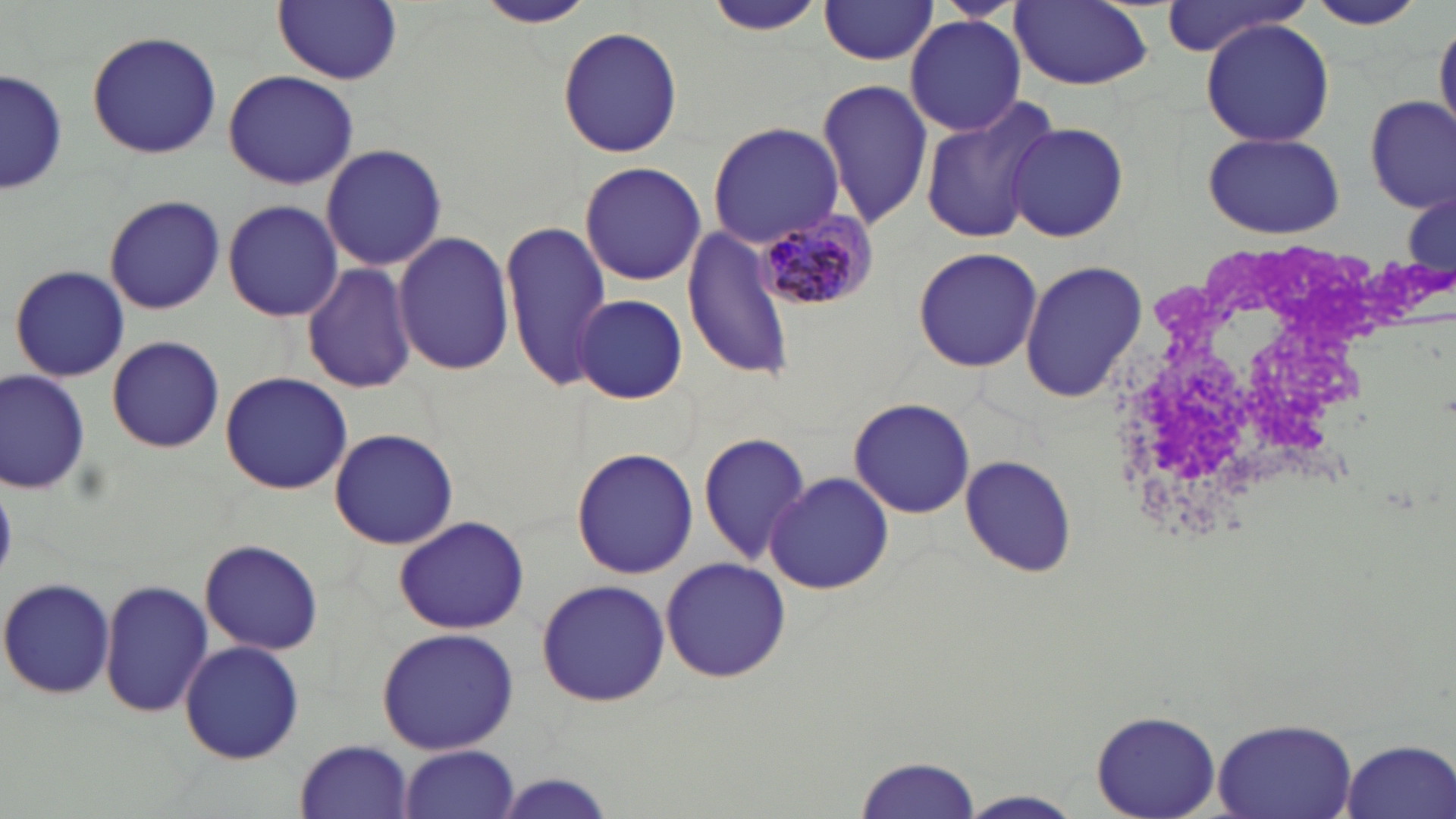 Approximate bounding boxes as named x1/y1/x2/y2 corners in pixels. Uninfected red blood cell locations: (x1=273, y1=0, x2=401, y2=86), (x1=1008, y1=0, x2=1155, y2=90), (x1=1301, y1=0, x2=1434, y2=32), (x1=478, y1=2, x2=596, y2=28), (x1=697, y1=2, x2=832, y2=36), (x1=817, y1=2, x2=939, y2=66), (x1=1158, y1=2, x2=1313, y2=61), (x1=904, y1=13, x2=1026, y2=136), (x1=1434, y1=15, x2=1456, y2=141), (x1=1201, y1=18, x2=1335, y2=148), (x1=557, y1=25, x2=683, y2=158), (x1=86, y1=29, x2=222, y2=159), (x1=2, y1=66, x2=65, y2=198), (x1=223, y1=69, x2=360, y2=191), (x1=815, y1=78, x2=936, y2=230), (x1=916, y1=96, x2=1061, y2=247), (x1=1364, y1=96, x2=1455, y2=214), (x1=706, y1=122, x2=845, y2=245), (x1=1006, y1=122, x2=1129, y2=243), (x1=1202, y1=130, x2=1347, y2=239), (x1=321, y1=142, x2=446, y2=273), (x1=578, y1=161, x2=707, y2=286), (x1=1402, y1=192, x2=1454, y2=276), (x1=103, y1=193, x2=225, y2=315), (x1=221, y1=199, x2=343, y2=321), (x1=499, y1=217, x2=612, y2=387), (x1=683, y1=229, x2=797, y2=383), (x1=392, y1=231, x2=515, y2=377), (x1=913, y1=245, x2=1042, y2=373), (x1=300, y1=261, x2=417, y2=394), (x1=1019, y1=261, x2=1148, y2=404), (x1=10, y1=265, x2=129, y2=383), (x1=575, y1=295, x2=686, y2=403), (x1=107, y1=335, x2=224, y2=453), (x1=0, y1=369, x2=89, y2=496), (x1=219, y1=371, x2=353, y2=496), (x1=848, y1=396, x2=977, y2=520), (x1=328, y1=426, x2=460, y2=548), (x1=697, y1=431, x2=810, y2=567), (x1=570, y1=446, x2=699, y2=579), (x1=959, y1=453, x2=1076, y2=578), (x1=763, y1=471, x2=892, y2=595), (x1=393, y1=515, x2=529, y2=635), (x1=198, y1=538, x2=326, y2=656), (x1=659, y1=557, x2=792, y2=684), (x1=0, y1=577, x2=118, y2=698), (x1=536, y1=577, x2=670, y2=708), (x1=99, y1=578, x2=214, y2=720), (x1=376, y1=628, x2=519, y2=754), (x1=180, y1=640, x2=304, y2=764), (x1=1092, y1=709, x2=1220, y2=818), (x1=1210, y1=715, x2=1360, y2=819), (x1=1337, y1=738, x2=1455, y2=818), (x1=296, y1=739, x2=415, y2=818), (x1=397, y1=745, x2=521, y2=819), (x1=854, y1=753, x2=983, y2=819), (x1=494, y1=773, x2=619, y2=819), (x1=957, y1=790, x2=1087, y2=818). Plasmodium malariae-infected red blood cell locations: (x1=747, y1=208, x2=876, y2=314). White blood cell locations: (x1=1103, y1=242, x2=1425, y2=549). Slide-level diagnosis: Plasmodium malariae. Thin blood smear. Image is 1456×819 pixels. May-Grünwald-Giemsa stain. Captured at 1000x magnification. Light microscopy. Single field of view.